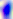
identification: Toxoplasma gondii
modality: photomicrograph
magnification: 400x